Locate every blood parasite and identify its species.
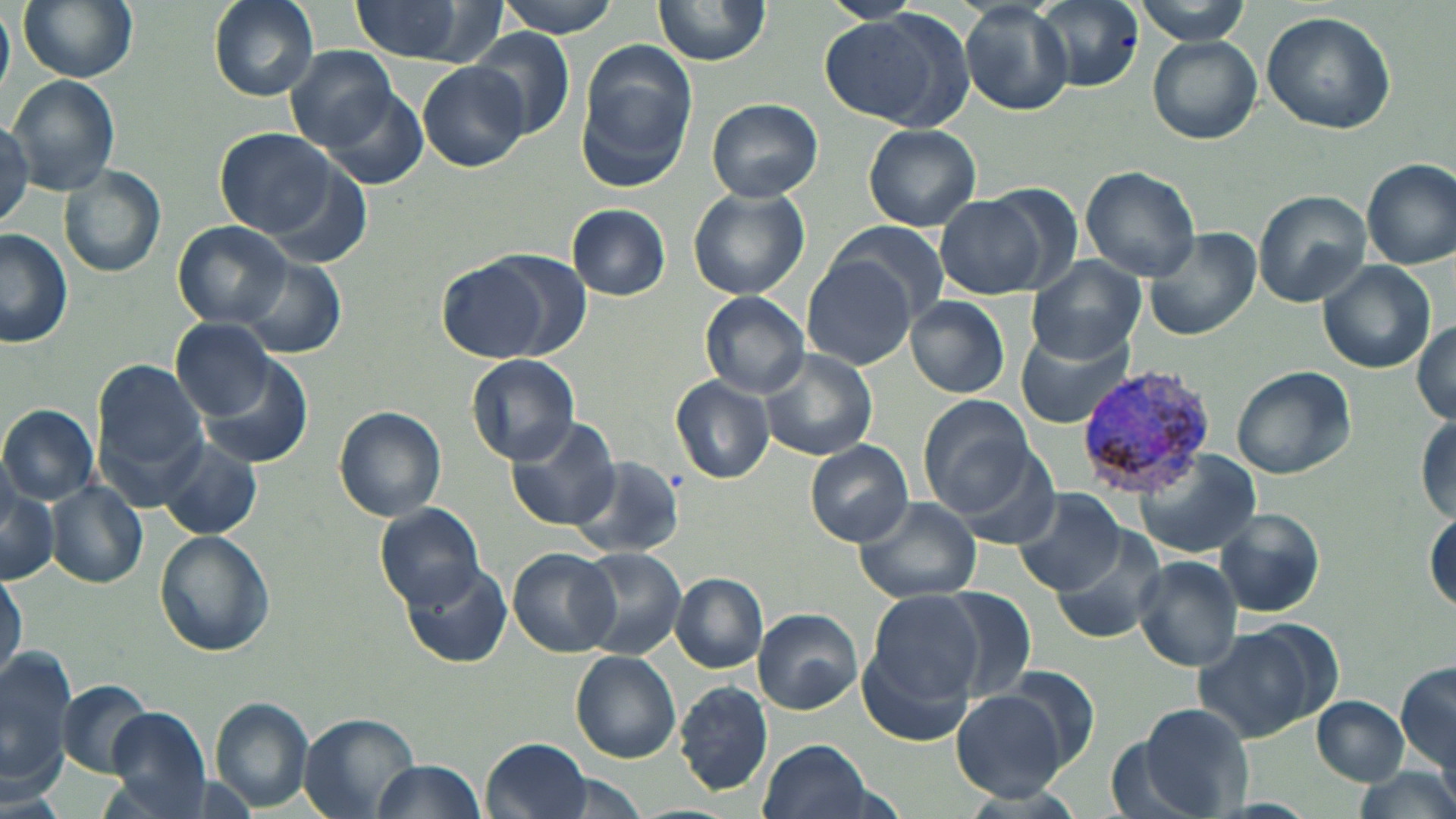

Approximate bounding boxes as (x1,y1)-(x2,y2) corner pairs in pixels.
Plasmodium vivax-infected red blood cells: (1078,364)-(1220,500).
No Plasmodium falciparum, Plasmodium ovale, Plasmodium malariae, Babesia divergens, or Trypanosoma brucei observed.

Uninfected red blood cell locations: (16,0)-(140,83), (207,0)-(318,101), (352,0)-(497,65), (495,0)-(625,37), (653,0)-(772,68), (821,0)-(924,24), (1031,0)-(1145,93), (1133,0)-(1253,43), (959,3)-(1074,115), (0,5)-(14,101), (1261,10)-(1397,136), (819,14)-(967,127), (470,29)-(576,143), (1145,34)-(1263,145), (576,38)-(696,191), (285,46)-(399,151), (417,59)-(528,172), (8,74)-(118,194), (311,79)-(432,193), (705,98)-(822,203), (0,116)-(32,231), (863,125)-(982,232), (213,127)-(343,239), (1361,160)-(1454,267), (60,166)-(167,278), (1079,166)-(1202,281), (687,186)-(811,300), (1252,190)-(1373,306), (937,194)-(1049,298), (567,203)-(671,301), (173,220)-(292,328), (825,222)-(947,325), (1142,226)-(1261,340), (0,229)-(74,350), (435,252)-(570,364), (802,256)-(919,370), (233,258)-(347,359), (1029,258)-(1144,363), (1317,261)-(1436,373), (700,292)-(809,397), (905,295)-(1010,398), (171,318)-(280,421), (1412,319)-(1456,427), (1016,328)-(1133,430), (760,351)-(879,460), (468,355)-(581,464), (196,357)-(315,468), (93,360)-(209,480), (1231,365)-(1357,480), (670,377)-(774,484), (921,396)-(1035,513), (0,404)-(98,504), (334,405)-(447,521), (1416,411)-(1455,522), (503,417)-(620,533), (155,438)-(265,542), (804,439)-(914,546), (945,440)-(1062,550), (1131,450)-(1263,559), (569,455)-(687,558), (46,480)-(149,589), (0,481)-(59,587), (1013,487)-(1130,594), (852,496)-(982,604), (376,504)-(487,610), (1214,508)-(1328,618), (1425,511)-(1456,614), (1048,527)-(1169,648), (154,529)-(275,658), (575,547)-(687,659), (508,548)-(623,657), (1132,556)-(1244,672), (402,560)-(511,667), (1,569)-(26,686), (671,573)-(768,672), (934,586)-(1038,705), (858,603)-(981,742), (752,608)-(863,714), (1193,622)-(1332,741), (0,646)-(72,797), (571,652)-(681,762), (1396,659)-(1455,778), (995,664)-(1099,772), (57,681)-(153,776), (675,681)-(773,795), (950,687)-(1073,798), (1312,695)-(1407,785), (210,696)-(314,812), (1131,704)-(1251,818), (103,706)-(214,816), (298,712)-(421,818), (483,735)-(591,818), (1107,737)-(1203,819), (758,738)-(876,819), (369,759)-(486,818), (1346,765)-(1456,819). Slide-level diagnosis: Plasmodium vivax. Image is 1456×819 pixels. Thin blood smear. Optical microscopy. One field of a larger specimen. May-Grünwald-Giemsa-stained preparation. 1000x magnification.